Comment on the morphology of the erythrocytes.
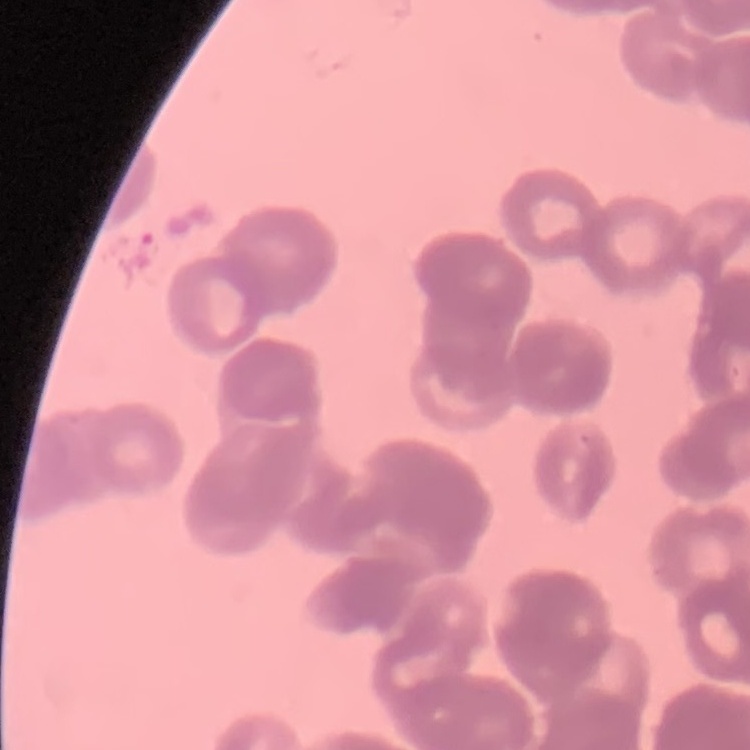

They show rouleaux formation.

stain = Field's or Giemsa
preparation = thin peripheral smear
image type = square crop of a larger photomicrograph